Outline each blood parasite and name the species.
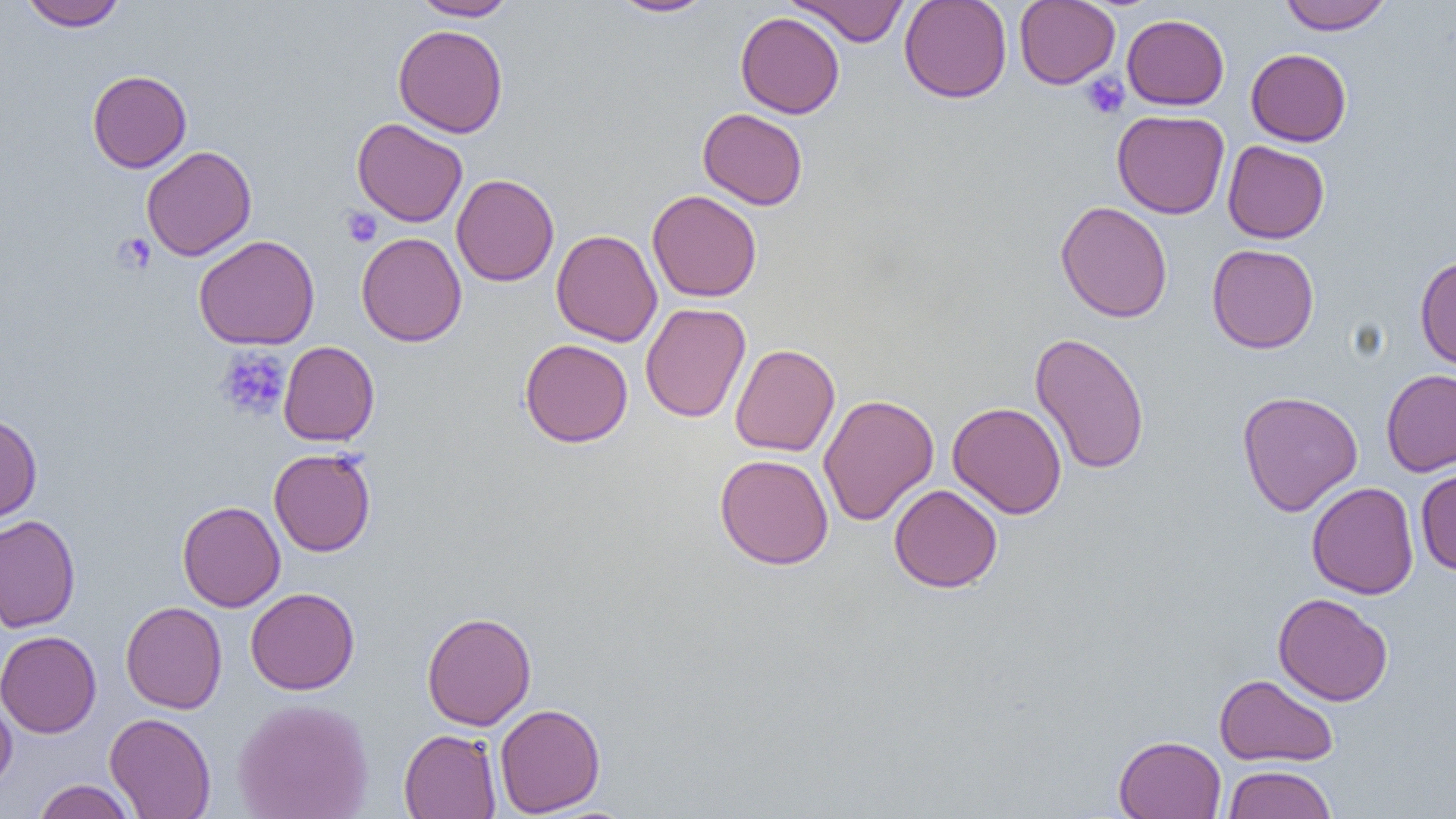
No blood parasites seen.

Summary:
  - Coordinate format: approximate bounding boxes as [x1, y1, x2, y2] in pixels
  - Platelet locations: [1081, 73, 1129, 119], [341, 206, 383, 248], [113, 232, 157, 275], [215, 346, 291, 421]
  - Uninfected red blood cell locations: [19, 0, 126, 30], [410, 0, 517, 20], [609, 0, 716, 17], [788, 0, 909, 46], [898, 0, 1012, 103], [1014, 0, 1120, 89], [1278, 0, 1393, 34], [735, 11, 845, 118], [1121, 14, 1229, 110], [393, 24, 508, 138], [1245, 48, 1352, 146], [87, 70, 191, 173], [697, 108, 808, 210], [1112, 110, 1230, 219], [352, 118, 468, 227], [1222, 140, 1330, 244], [141, 145, 256, 261], [452, 174, 559, 287], [647, 190, 762, 302], [1056, 201, 1172, 323], [550, 229, 662, 346], [356, 232, 467, 347], [194, 234, 320, 350], [1207, 244, 1319, 353], [1415, 254, 1456, 371], [639, 302, 751, 423], [1030, 332, 1149, 475], [519, 339, 633, 447], [278, 341, 379, 446], [730, 343, 840, 456], [1381, 369, 1456, 476], [1237, 390, 1363, 516], [819, 393, 938, 526], [948, 401, 1067, 519], [0, 411, 42, 524], [269, 448, 376, 556], [715, 453, 834, 570], [1415, 466, 1456, 575], [1306, 482, 1419, 599], [888, 484, 1003, 592], [177, 500, 285, 612], [0, 515, 80, 632], [246, 587, 360, 694], [1272, 592, 1393, 706], [121, 600, 227, 714], [422, 611, 537, 730], [0, 630, 102, 738], [1214, 673, 1339, 767], [0, 694, 17, 793], [231, 697, 374, 819], [494, 703, 606, 817], [105, 712, 216, 819], [399, 728, 501, 819], [1114, 735, 1227, 819], [1221, 764, 1337, 819], [32, 779, 138, 819]
  - Slide-level diagnosis: no evidence of blood parasites
  - Image size: 1456×819 pixels
  - Field of view: single
  - Preparation: thin blood film
  - Modality: optical microscopy
  - Magnification: 1000x